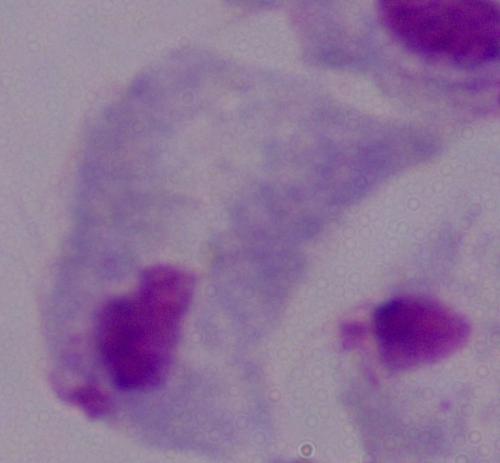
A trichomonad is seen. Photomicrograph. Captured at 1000x magnification.